Classify this cell by malaria status.
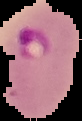

It is parasitized.

Summary:
  - Image size: 82×121 pixels
  - Preparation: thin blood smear
  - Image type: cell region segmented out of the field of view; surrounding area masked to black